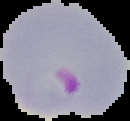
From a thin blood smear. The area outside the segmented cell region is set to black. Image is 130×121 pixels. Result: malaria parasites detected.